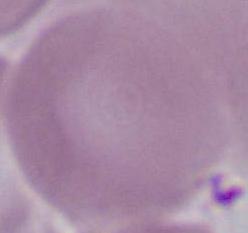

A red blood cell is shown. Captured at 1000x magnification. Photomicrograph.